Identify the parasite.
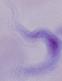

A trypanosome.

Photomicrograph. Captured at 1000x magnification.